Locate and identify every blood parasite.
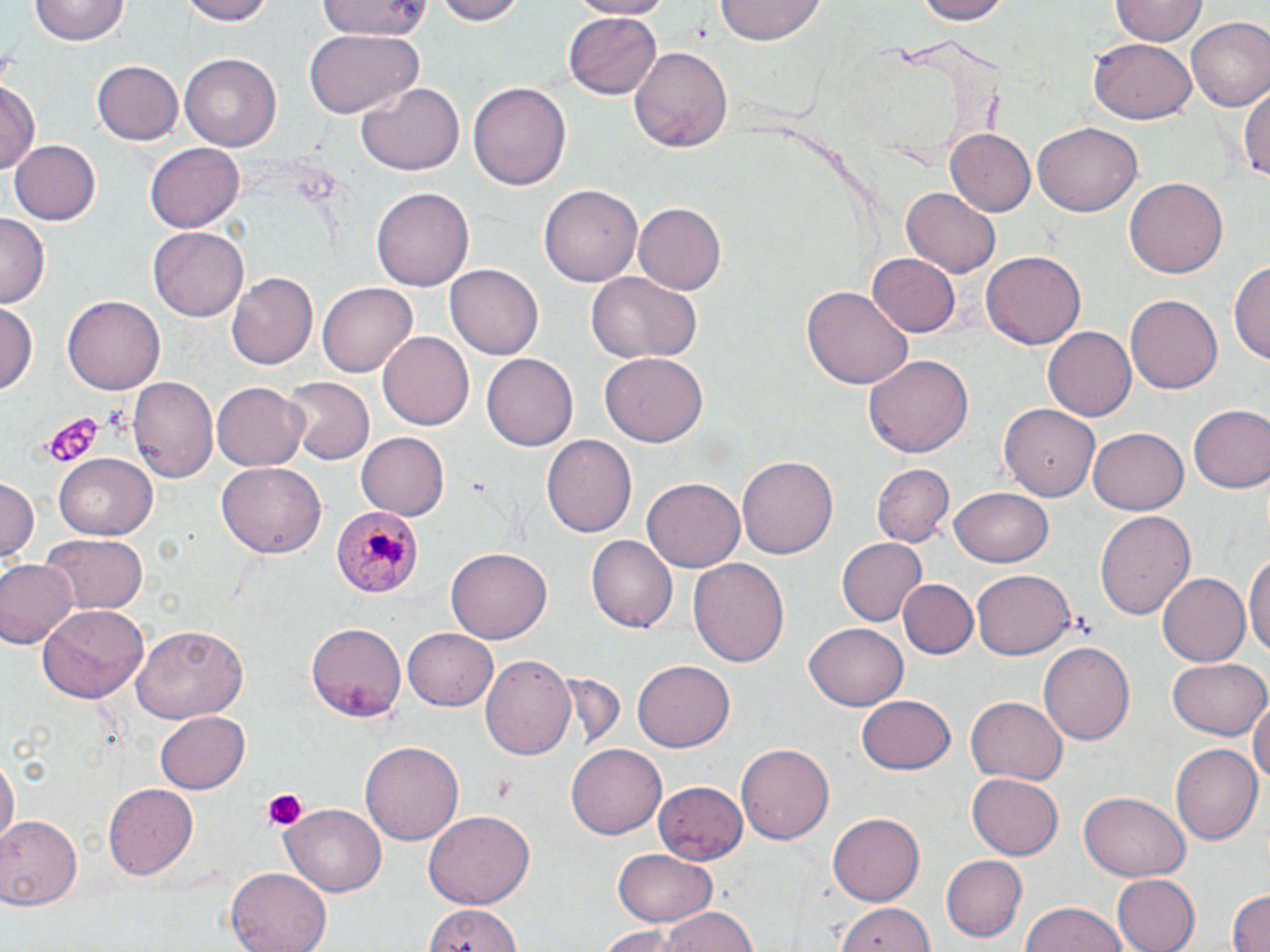
Approximate bounding boxes as (x1,y1)-(x2,y2) corner pairs in pixels.
Plasmodium malariae-infected red blood cells: (330,507)-(423,600).
No Plasmodium falciparum, Plasmodium ovale, Plasmodium vivax, Babesia divergens, or Trypanosoma brucei observed.

Platelet locations: (40,410)-(105,469), (491,774)-(517,807), (258,788)-(311,833). Uninfected red blood cell locations: (178,0)-(279,25), (315,0)-(435,42), (428,0)-(525,25), (570,0)-(678,18), (911,0)-(1014,24), (31,1)-(130,47), (714,2)-(828,45), (1111,2)-(1208,46), (565,13)-(661,99), (1185,17)-(1270,112), (303,29)-(421,116), (1090,39)-(1198,124), (630,46)-(734,154), (180,53)-(280,152), (92,60)-(184,144), (1,79)-(42,175), (470,79)-(570,193), (355,80)-(465,177), (1240,83)-(1269,187), (1032,123)-(1140,217), (945,129)-(1035,217), (11,138)-(101,225), (145,142)-(245,232), (1125,177)-(1227,279), (371,183)-(471,290), (540,183)-(643,287), (902,187)-(1001,276), (634,203)-(725,293), (0,216)-(48,306), (148,227)-(249,321), (981,252)-(1085,349), (866,253)-(960,337), (1231,259)-(1270,372), (448,263)-(542,359), (585,270)-(703,365), (226,272)-(319,369), (318,282)-(417,379), (800,285)-(913,391), (1125,295)-(1224,395), (63,296)-(166,394), (1,303)-(38,394), (1042,326)-(1135,421), (379,331)-(473,431), (482,351)-(578,452), (601,352)-(709,447), (865,354)-(975,460), (129,377)-(218,483), (281,377)-(371,465), (212,382)-(309,470), (1002,401)-(1102,499), (1188,406)-(1269,493), (1088,427)-(1188,514), (357,431)-(449,520), (544,433)-(638,537), (736,452)-(836,556), (56,454)-(157,536), (218,461)-(328,558), (871,462)-(954,545), (1,476)-(39,568), (641,479)-(744,572), (951,489)-(1052,566), (1094,510)-(1196,620), (36,534)-(149,614), (586,534)-(678,633), (836,536)-(928,627), (448,548)-(551,643), (1244,552)-(1270,660), (689,556)-(789,672), (0,561)-(76,649), (971,570)-(1074,659), (1158,573)-(1250,665), (899,579)-(975,658), (36,604)-(149,704), (306,621)-(406,721), (806,621)-(908,712), (132,625)-(250,722), (403,629)-(501,710), (1039,640)-(1134,748), (482,654)-(577,762), (1168,658)-(1269,741), (632,659)-(734,751), (857,693)-(956,774), (1251,693)-(1270,797), (964,697)-(1067,787), (155,708)-(250,792), (358,739)-(464,845), (737,740)-(833,841), (1169,742)-(1262,845), (568,744)-(666,840), (0,755)-(16,853), (967,770)-(1067,860), (653,780)-(749,862), (104,784)-(199,880), (1079,793)-(1188,880), (282,801)-(389,896), (424,809)-(535,908), (828,813)-(925,903), (0,816)-(81,911), (612,847)-(717,927), (942,855)-(1028,941), (228,866)-(332,952), (1110,875)-(1200,952), (1226,888)-(1270,952), (837,902)-(934,952), (1019,902)-(1128,952), (423,905)-(525,952), (656,908)-(760,952), (588,925)-(689,950). Slide-level diagnosis: Plasmodium malariae. Single field of view. Image is 1270×952 pixels. Optical microscopy. Captured at 1000x magnification. Thin blood film. May-Grünwald-Giemsa-stained preparation.